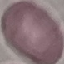
Malaria status: uninfected. Giemsa-stained preparation. Acquired by smartphone through the microscope eyepiece. Thin blood smear. Automatically extracted cell patch, resized to 64 × 64 pixels.